Locate every Plasmodium malariae-infected red blood cell.
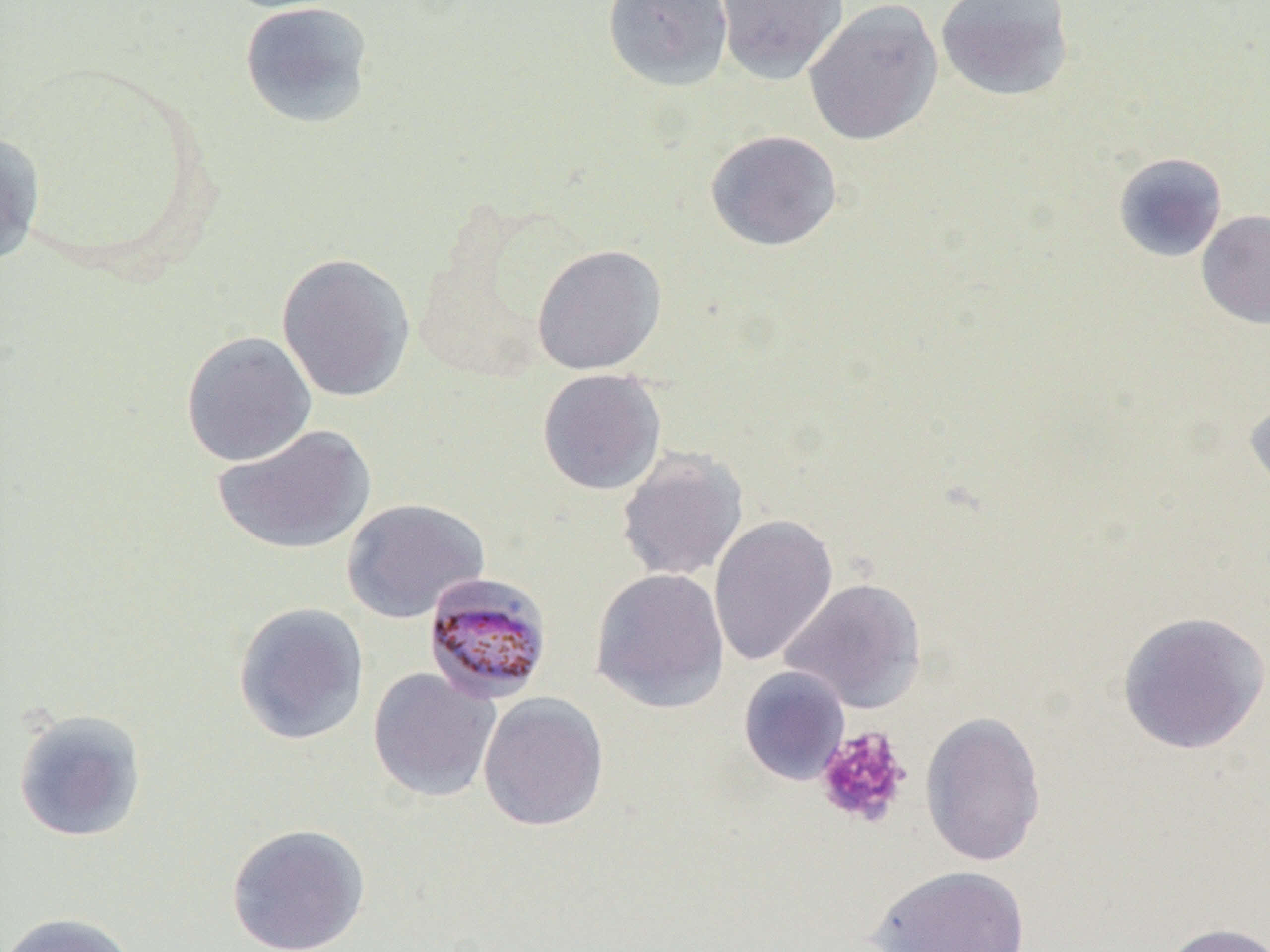
Approximate bounding boxes as (x1, y1, x2, y2) in pixels.
Plasmodium malariae-infected red blood cells: (423, 572, 554, 704).

Platelet locations: (814, 725, 912, 829). Uninfected red blood cell locations: (213, 0, 351, 14), (601, 0, 734, 92), (715, 0, 849, 84), (802, 0, 943, 147), (935, 0, 1075, 102), (239, 1, 375, 129), (704, 130, 844, 252), (0, 131, 46, 266), (1112, 152, 1228, 263), (1196, 210, 1270, 330), (531, 244, 667, 375), (276, 252, 416, 403), (181, 330, 317, 467), (537, 368, 667, 496), (1244, 392, 1270, 501), (211, 423, 377, 556), (615, 448, 749, 582), (341, 497, 490, 624), (709, 514, 838, 668), (589, 567, 731, 713), (780, 577, 927, 714), (233, 601, 370, 746), (1116, 611, 1270, 755), (738, 666, 851, 786), (367, 667, 501, 803), (478, 691, 609, 832), (13, 708, 148, 843), (919, 710, 1047, 867), (226, 822, 371, 952), (869, 864, 1029, 952), (1, 911, 140, 952), (1159, 921, 1270, 952). Slide-level diagnosis: Plasmodium malariae. Optical microscopy. Thin blood smear. Single field of view. Image is 1270×952 pixels. 1000x magnification.